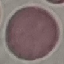

Summary:
  - Malaria status: uninfected
  - Image type: cell patch, automatically extracted from a larger field of view and resized to 64 × 64 pixels
  - Preparation: thin blood film
  - Stain: Giemsa
  - Capture: smartphone camera at the microscope eyepiece